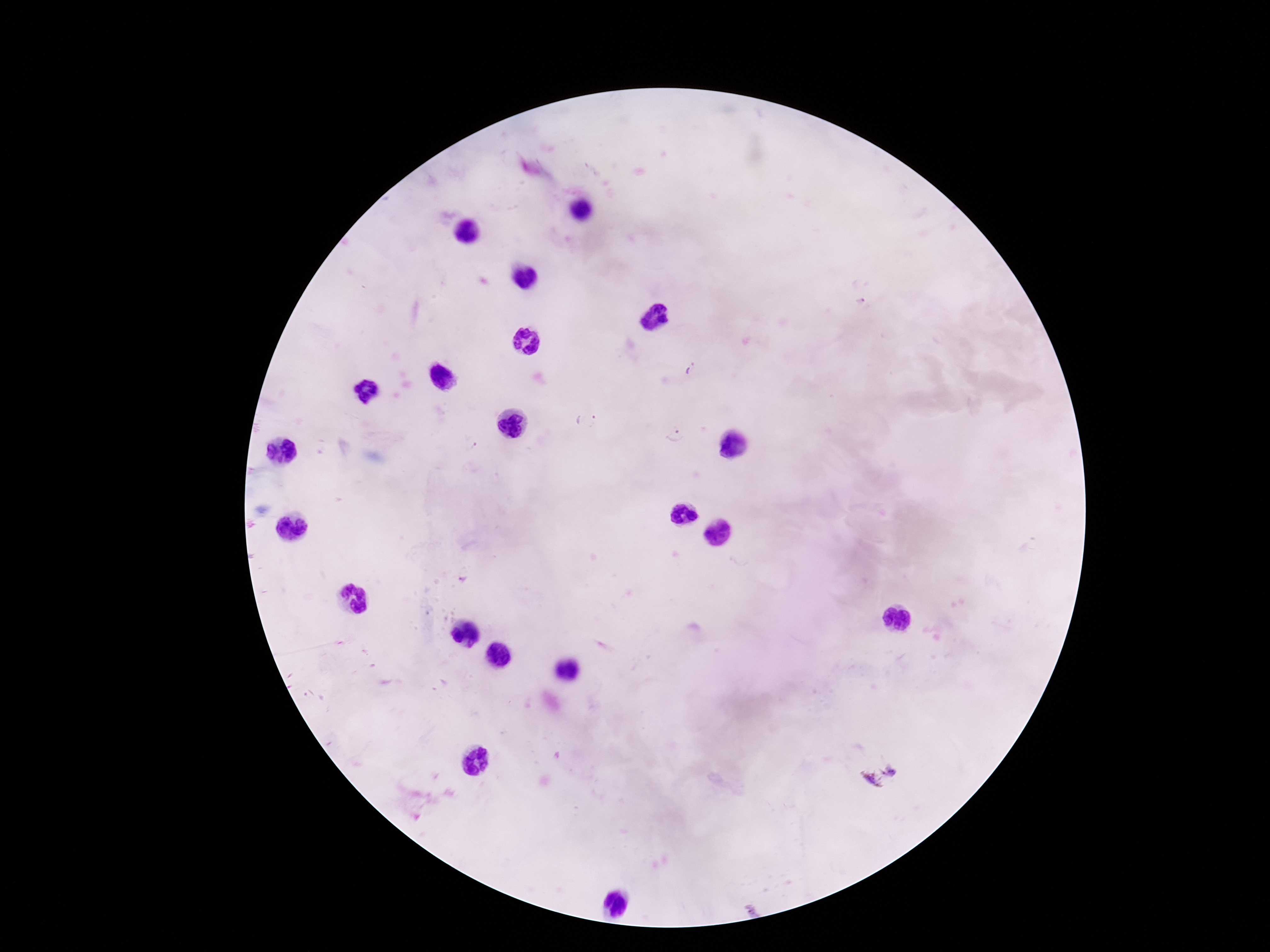
Approximate centers as {x, y} in pixels.
Summary:
  - Plasmodium parasite locations: {859, 301}, {691, 371}, {586, 421}, {673, 435}, {473, 446}, {463, 580}, {879, 778}
  - Stain: Giemsa
  - Field of view: single
  - Patient malaria status: infected
  - Image size: 1270×952 pixels
  - Capture: smartphone camera through the microscope eyepiece
  - Magnification: 100x
  - Preparation: thick blood smear